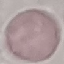

Result: no malaria parasites seen. Giemsa stain. Cell patch, automatically extracted from a larger field of view and resized to 64 × 64 pixels. Photographed with a smartphone camera at the microscope eyepiece. Thin smear of blood.